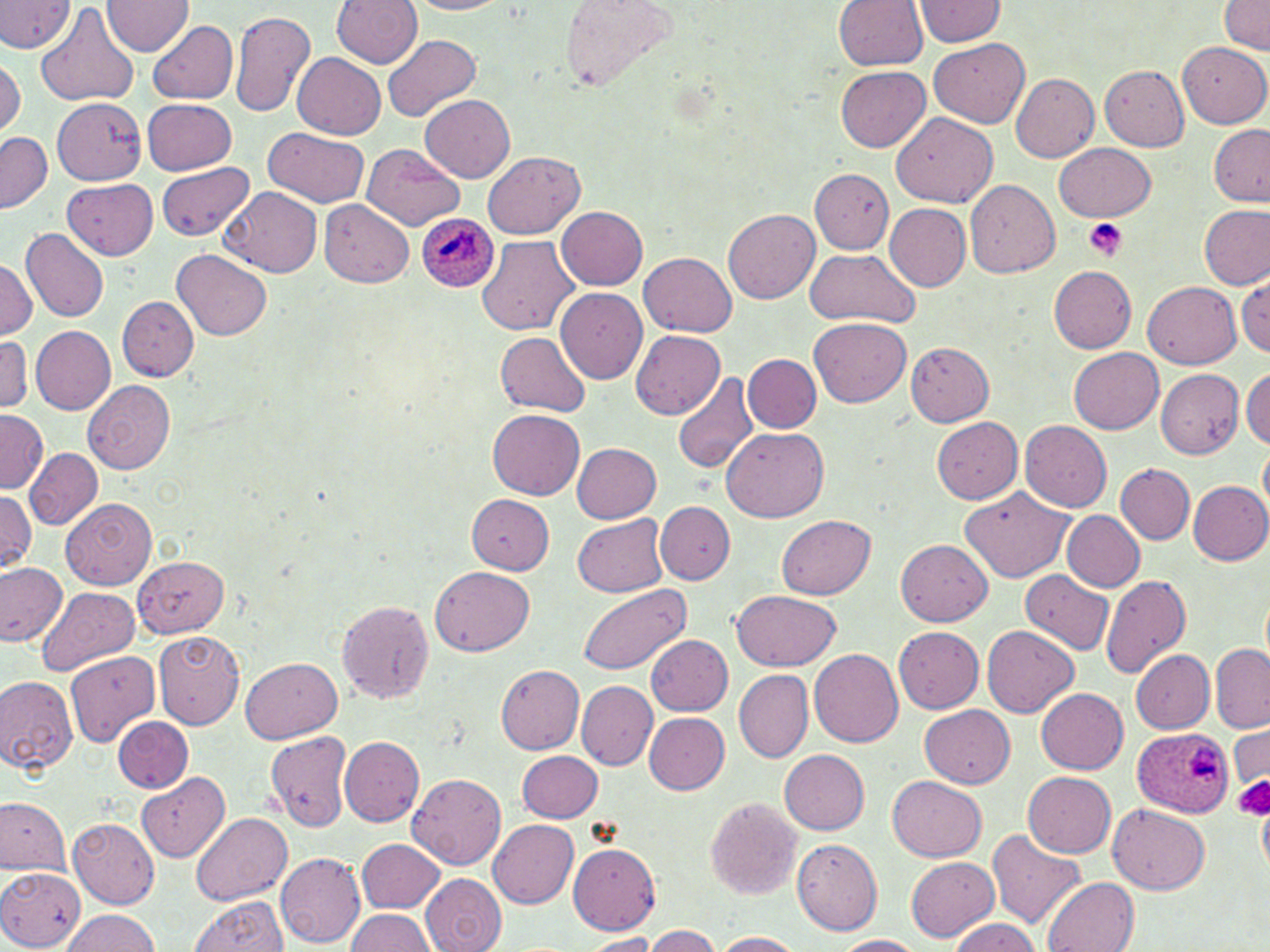
Approximate bounding boxes as (x1,y1)-(x2,y2) corner pairs in pixels. Platelet locations: (1084,217)-(1127,261), (1234,775)-(1270,820). Plasmodium ovale-infected red blood cell locations: (415,214)-(500,293), (1132,727)-(1234,817). Uninfected red blood cell locations: (0,0)-(76,54), (103,0)-(194,56), (332,0)-(424,68), (562,0)-(679,93), (834,0)-(929,71), (911,0)-(1007,46), (412,1)-(509,15), (1217,1)-(1270,56), (36,3)-(139,107), (229,9)-(315,118), (147,19)-(239,104), (383,35)-(480,121), (928,38)-(1030,129), (1178,41)-(1270,128), (293,52)-(386,139), (1,56)-(25,137), (835,64)-(931,152), (1100,65)-(1190,151), (1011,73)-(1099,162), (420,93)-(516,183), (55,97)-(146,183), (141,98)-(236,174), (890,112)-(999,207), (1208,124)-(1270,206), (263,127)-(368,206), (1,131)-(52,212), (1056,142)-(1156,223), (361,143)-(465,231), (483,151)-(585,240), (156,161)-(255,240), (810,168)-(893,254), (62,177)-(157,260), (964,178)-(1061,277), (223,187)-(322,277), (320,199)-(415,288), (885,204)-(971,291), (1199,204)-(1268,290), (556,206)-(647,290), (723,209)-(819,303), (22,228)-(109,322), (477,235)-(578,337), (173,249)-(272,340), (803,250)-(921,327), (641,252)-(736,337), (0,259)-(36,339), (1047,264)-(1138,354), (1234,272)-(1270,357), (1144,281)-(1241,369), (556,288)-(647,386), (117,296)-(199,381), (809,317)-(911,407), (31,326)-(116,415), (631,329)-(726,418), (495,331)-(591,418), (0,335)-(32,414), (904,340)-(995,425), (1069,348)-(1164,434), (743,354)-(821,432), (1242,365)-(1270,449), (1154,368)-(1244,457), (672,371)-(760,475), (84,380)-(175,474), (0,409)-(47,493), (487,409)-(585,500), (931,415)-(1023,504), (1020,419)-(1113,511), (723,427)-(828,521), (1259,440)-(1270,521), (572,441)-(662,521), (26,449)-(102,528), (1116,463)-(1194,544), (1186,480)-(1270,565), (959,485)-(1073,582), (0,488)-(39,576), (467,494)-(555,575), (61,498)-(157,590), (656,502)-(734,584), (1061,510)-(1145,592), (572,514)-(668,598), (777,514)-(875,599), (897,539)-(992,624), (133,556)-(229,637), (0,563)-(68,648), (430,566)-(535,655), (1021,569)-(1114,657), (1099,575)-(1192,679), (576,582)-(689,675), (36,587)-(140,676), (730,589)-(843,670), (1261,589)-(1269,667), (335,597)-(437,704), (982,625)-(1080,717), (894,627)-(983,712), (154,629)-(244,729), (646,634)-(733,716), (1209,644)-(1270,733), (809,648)-(905,748), (1130,649)-(1214,733), (67,651)-(159,747), (241,658)-(344,743), (495,664)-(586,754), (733,669)-(813,764), (0,673)-(79,773), (576,680)-(656,770), (1036,687)-(1129,772), (920,705)-(1014,788), (644,712)-(730,794), (113,717)-(192,792), (1229,725)-(1269,788), (265,729)-(354,834), (340,737)-(423,827), (517,749)-(603,823), (780,749)-(870,834), (407,772)-(506,870), (1024,772)-(1116,858), (137,773)-(229,862), (889,775)-(987,861), (705,797)-(801,900), (0,798)-(70,876), (1109,804)-(1211,895), (1259,805)-(1270,875), (191,813)-(292,906), (69,818)-(159,908), (489,819)-(580,909), (987,830)-(1086,931), (357,838)-(445,912), (791,839)-(882,935), (567,844)-(661,932), (276,852)-(366,948), (904,856)-(999,942), (0,866)-(85,950), (420,873)-(507,952), (1042,876)-(1139,952), (189,896)-(289,952), (59,908)-(161,952), (345,909)-(436,952), (947,916)-(1043,952), (644,926)-(721,951), (710,931)-(804,951), (583,933)-(660,950), (832,935)-(928,952). Slide-level diagnosis: Plasmodium ovale. Thin blood smear. Optical microscopy. May-Grünwald-Giemsa stain. 1000x magnification. Image is 1270×952 pixels. Single field of view.